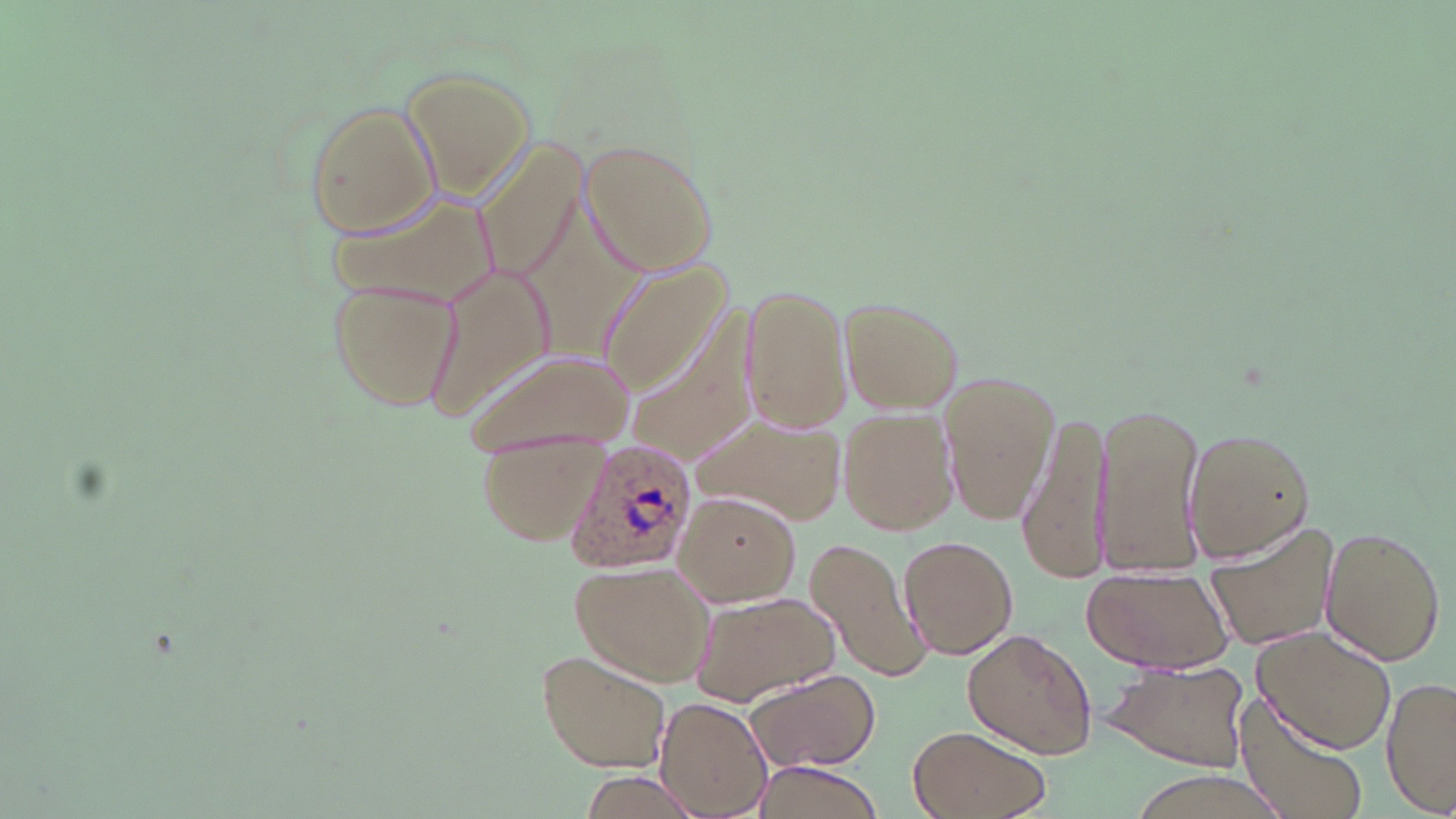
Approximate bounding boxes as (x1, y1, x2, y2) in pixels. Plasmodium ovale-infected red blood cell locations: (559, 438, 696, 576). Uninfected red blood cell locations: (399, 65, 536, 195), (304, 100, 442, 237), (467, 131, 589, 293), (578, 139, 718, 276), (513, 188, 640, 370), (328, 189, 495, 320), (599, 262, 730, 392), (420, 263, 552, 425), (325, 277, 461, 412), (741, 284, 850, 435), (835, 295, 966, 416), (624, 302, 762, 469), (465, 347, 633, 457), (941, 370, 1060, 525), (1091, 401, 1206, 578), (838, 409, 959, 537), (698, 411, 846, 525), (1019, 412, 1110, 586), (1181, 426, 1319, 563), (475, 432, 605, 546), (672, 491, 799, 606), (1202, 520, 1337, 653), (1318, 523, 1446, 667), (898, 534, 1018, 659), (804, 535, 931, 683), (569, 561, 712, 684), (1079, 570, 1234, 674), (689, 590, 840, 705), (1253, 623, 1397, 755), (960, 627, 1098, 759), (536, 651, 673, 772), (1102, 657, 1252, 773), (742, 670, 880, 771), (1382, 676, 1455, 818), (1236, 694, 1373, 819), (655, 697, 773, 818), (907, 727, 1052, 819), (750, 760, 886, 818), (576, 772, 701, 819), (1123, 772, 1295, 817). Slide-level diagnosis: Plasmodium ovale. Light microscopy. One field of a larger specimen. Image is 1456×819 pixels. 1000x magnification. May-Grünwald-Giemsa stain. Thin blood smear.